Locate and identify every blood parasite.
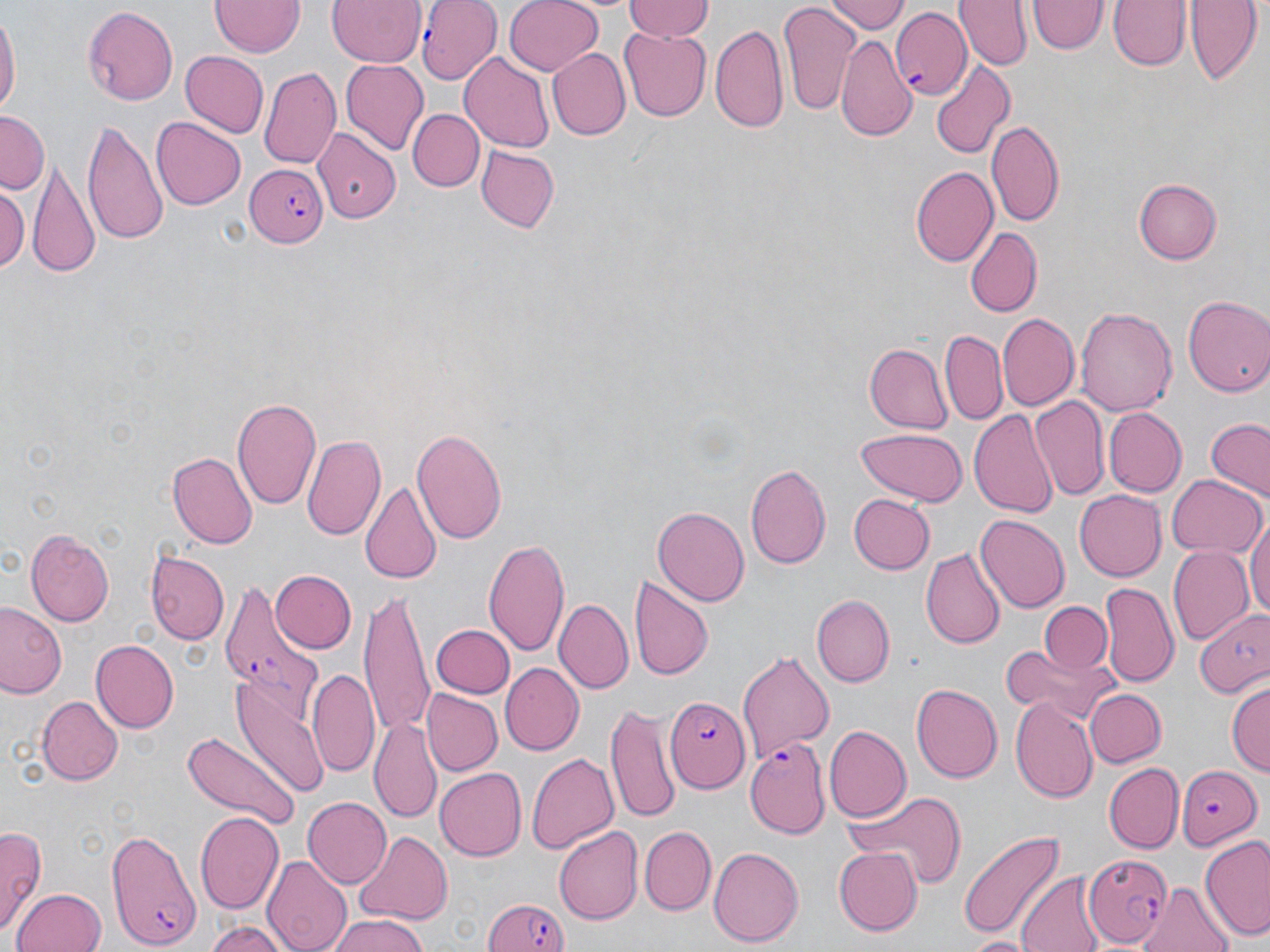

Approximate bounding boxes as (x1, y1, x2, y2) in pixels.
Plasmodium falciparum-infected red blood cells: (417, 1, 498, 85), (890, 9, 970, 104), (309, 126, 400, 228), (245, 164, 327, 249), (219, 580, 323, 728), (663, 696, 749, 791), (745, 738, 831, 837), (1176, 761, 1260, 850), (105, 825, 200, 949), (1083, 850, 1173, 948), (480, 894, 572, 952).
No Plasmodium ovale, Plasmodium malariae, Plasmodium vivax, Babesia divergens, or Trypanosoma brucei observed.

Summary:
  - Uninfected red blood cell locations: (327, 0, 427, 67), (503, 0, 604, 76), (621, 0, 715, 42), (829, 0, 905, 34), (956, 0, 1031, 70), (1107, 0, 1192, 73), (1187, 0, 1261, 84), (209, 1, 303, 57), (1030, 1, 1106, 56), (779, 4, 862, 120), (82, 5, 179, 106), (0, 13, 20, 115), (710, 21, 791, 134), (619, 27, 713, 121), (838, 34, 917, 144), (548, 48, 630, 141), (182, 50, 267, 138), (460, 52, 556, 152), (342, 59, 429, 155), (930, 59, 1015, 159), (259, 65, 342, 168), (409, 107, 483, 192), (0, 111, 47, 196), (151, 117, 247, 209), (987, 119, 1066, 227), (82, 121, 167, 243), (475, 145, 558, 233), (29, 163, 99, 276), (913, 166, 999, 266), (926, 178, 1037, 292), (1135, 178, 1222, 263), (0, 185, 30, 273), (962, 226, 1045, 316), (1183, 296, 1270, 399), (1075, 304, 1176, 419), (998, 312, 1080, 412), (939, 327, 1007, 426), (865, 342, 952, 431), (1031, 393, 1109, 503), (232, 394, 323, 513), (1106, 408, 1187, 496), (968, 409, 1057, 518), (1204, 419, 1269, 502), (411, 426, 508, 545), (856, 427, 964, 505), (303, 434, 386, 542), (169, 453, 256, 550), (744, 462, 832, 573), (1167, 474, 1265, 558), (362, 479, 443, 588), (1072, 489, 1165, 582), (849, 494, 934, 573), (653, 505, 749, 605), (1247, 510, 1270, 627), (975, 515, 1069, 613), (25, 527, 115, 625), (483, 535, 570, 657), (146, 545, 229, 647), (1168, 547, 1253, 646), (920, 548, 1004, 651), (269, 568, 357, 656), (631, 578, 713, 682), (1099, 583, 1178, 687), (362, 595, 432, 740), (812, 595, 894, 686), (556, 599, 633, 694), (1039, 600, 1112, 674), (0, 602, 66, 701), (1194, 609, 1270, 699), (432, 622, 512, 698), (90, 639, 178, 733), (1000, 644, 1104, 721), (739, 650, 835, 764), (501, 662, 585, 755), (308, 668, 380, 780), (231, 675, 329, 800), (1227, 682, 1270, 777), (911, 684, 1005, 782), (1085, 688, 1166, 769), (423, 689, 502, 775), (38, 694, 123, 785), (1009, 695, 1098, 801), (607, 704, 681, 826), (371, 718, 442, 826), (823, 725, 911, 823), (183, 729, 300, 831), (528, 751, 622, 855), (1105, 763, 1183, 852), (436, 768, 525, 860), (842, 790, 966, 888), (303, 797, 391, 887), (194, 813, 285, 915), (0, 825, 44, 939), (639, 826, 716, 915), (554, 827, 642, 923), (957, 828, 1065, 944), (354, 830, 451, 924), (1200, 838, 1270, 940), (708, 847, 803, 946), (833, 848, 924, 935), (264, 853, 351, 952), (1017, 872, 1105, 952), (1141, 884, 1234, 952), (9, 889, 106, 952), (329, 914, 430, 952), (205, 919, 291, 952), (961, 934, 1035, 951)
  - Slide-level diagnosis: Plasmodium falciparum
  - Preparation: thin blood smear
  - Image size: 1270×952 pixels
  - Field of view: one of a larger specimen
  - Magnification: 1000x
  - Modality: optical microscopy
  - Stain: May-Grünwald-Giemsa